Assess the morphology of the red blood cells.
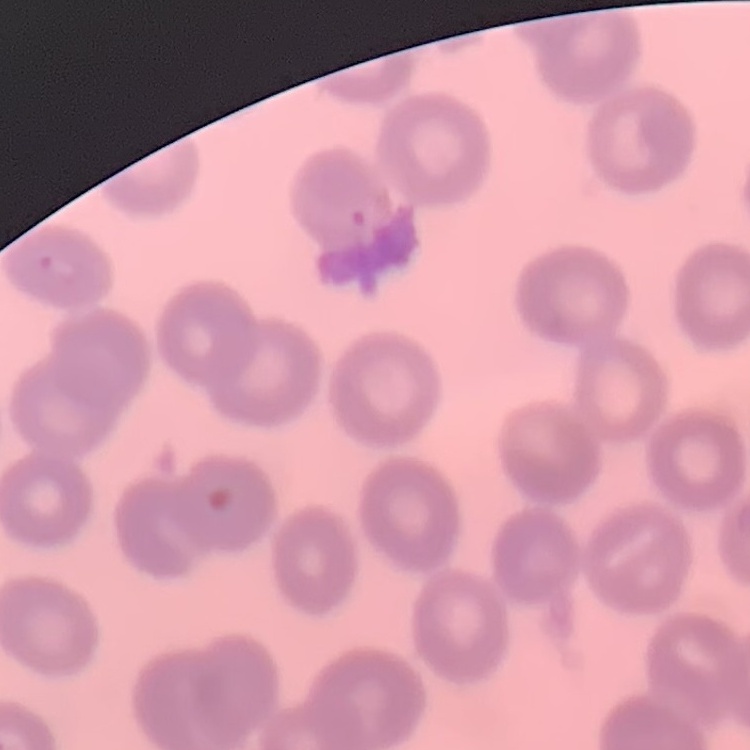

No rouleaux formation.

image type = one tile cut from a larger photomicrograph
preparation = thin blood smear
stain = Field's or Giemsa